Classify this cell by malaria status.
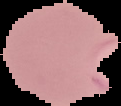
It is parasitized.

image_size: 121×106 pixels
preparation: thin blood film
image_type: segmented cell region on a black background